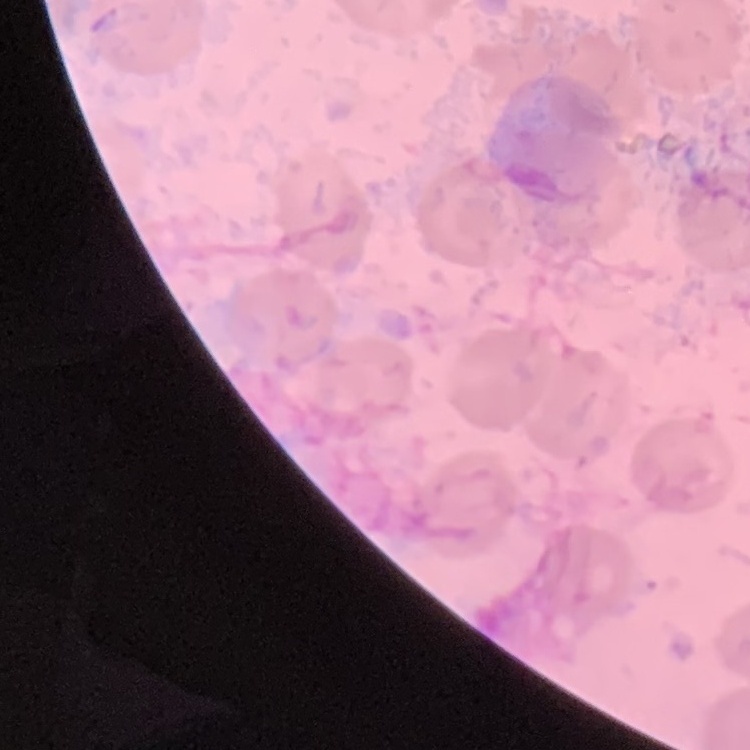

red blood cell morphology = no rouleaux formation
preparation = thin peripheral smear
stain = Field's or Giemsa
image type = square crop of a larger photomicrograph